Assess this cell for malaria.
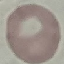
It is uninfected.

capture: smartphone camera at the microscope eyepiece
image_type: cell patch, automatically extracted from a larger field of view and resized to 64 × 64 pixels
stain: Giemsa
preparation: thin blood film